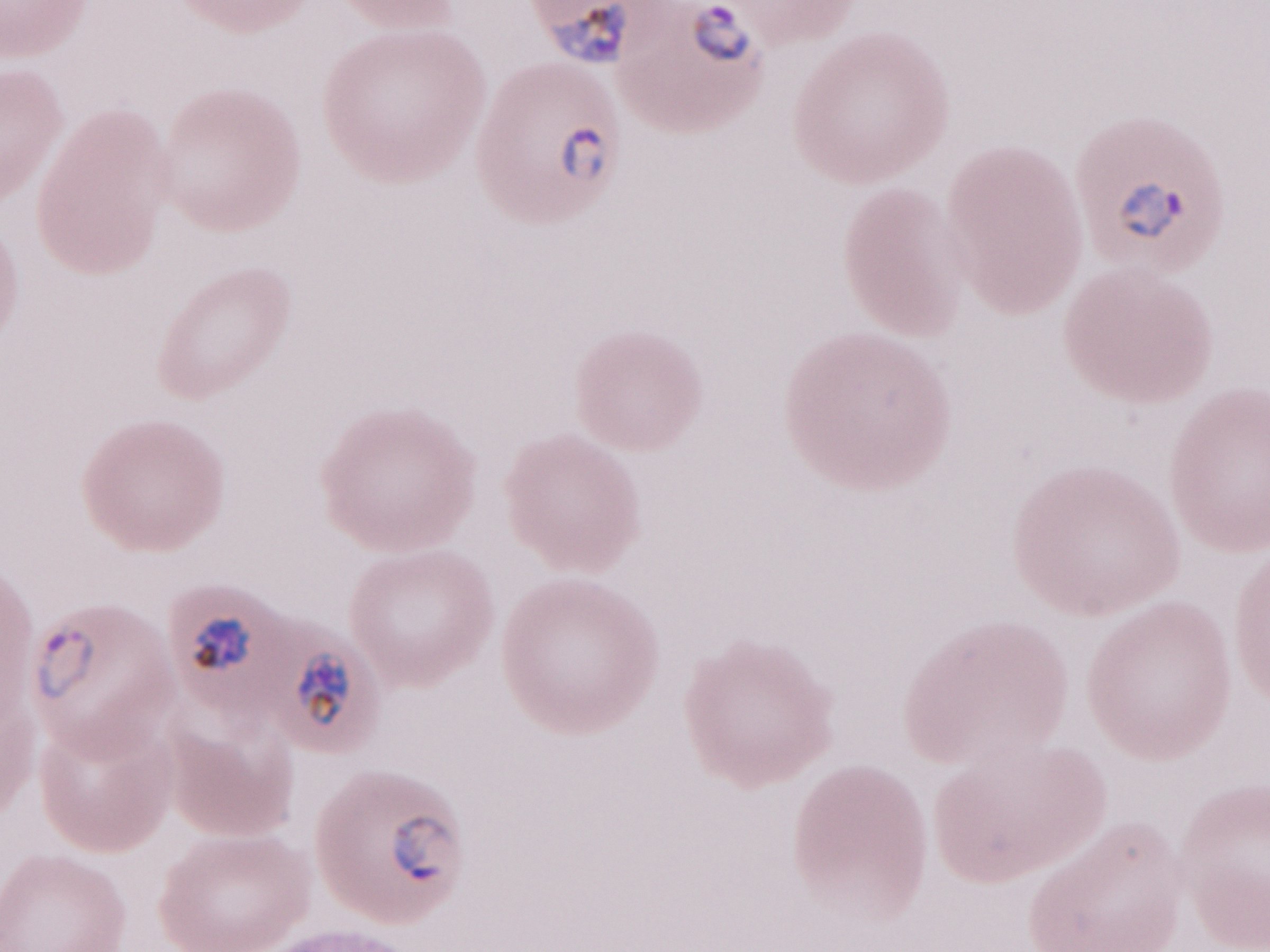
Patient diagnosis: malaria infection. Olympus BX43 microscope, Olympus DP73 camera. Image is 1270×952 pixels. Magnification: 1,000x. May-Grünwald-Giemsa-stained preparation. One field of this slide. Thin peripheral-blood smear.